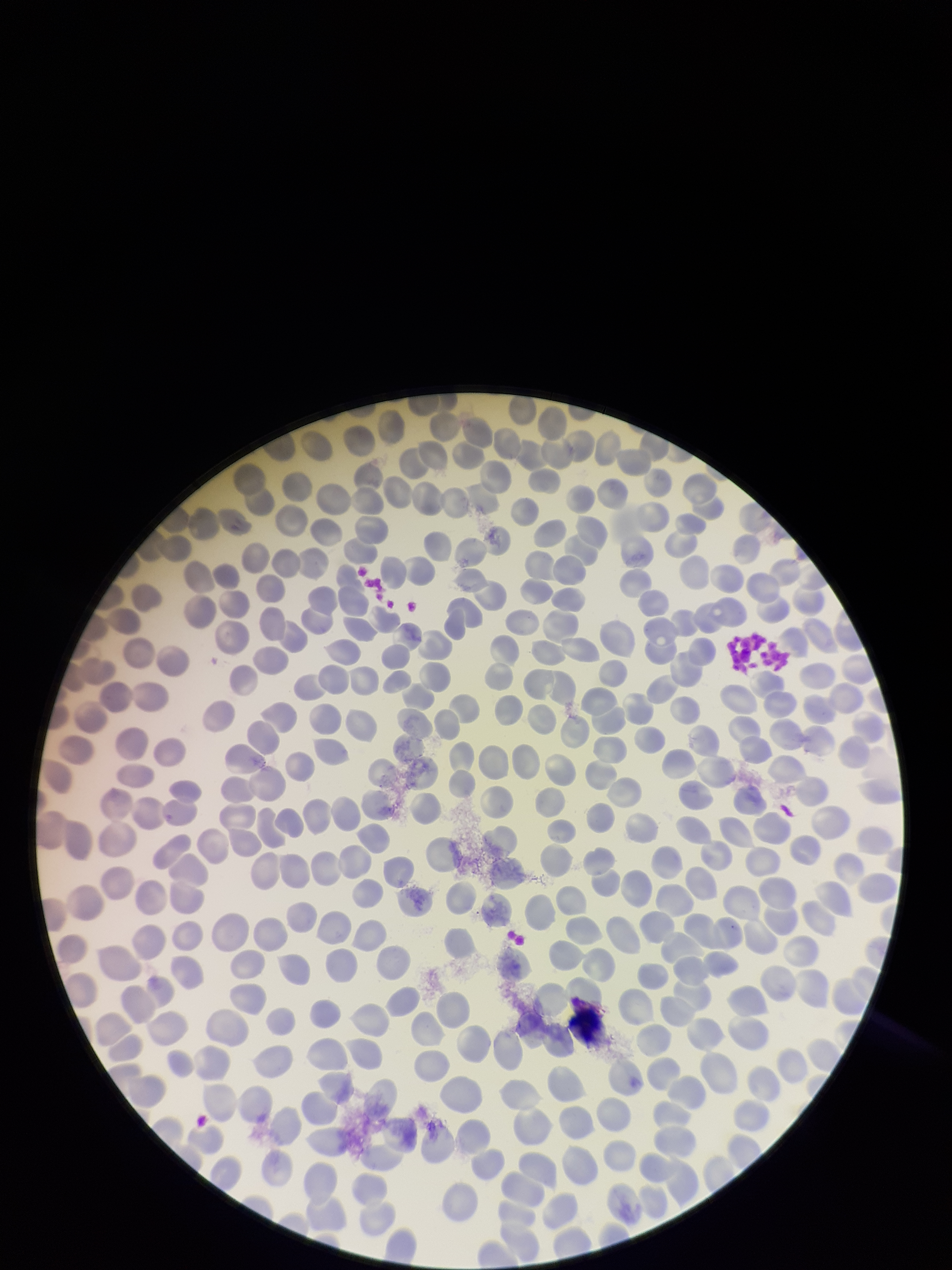

Summary:
  - Preparation: thin
  - Field of view: one from this slide
  - Red blood cell count: 347
  - Stain: Giemsa
  - Parasitized red blood cells: none identified
  - Capture: smartphone photograph through the microscope eyepiece
  - Parasitized red blood cell count: 0
  - Image size: 952×1270 pixels
  - Patient malaria status: negative